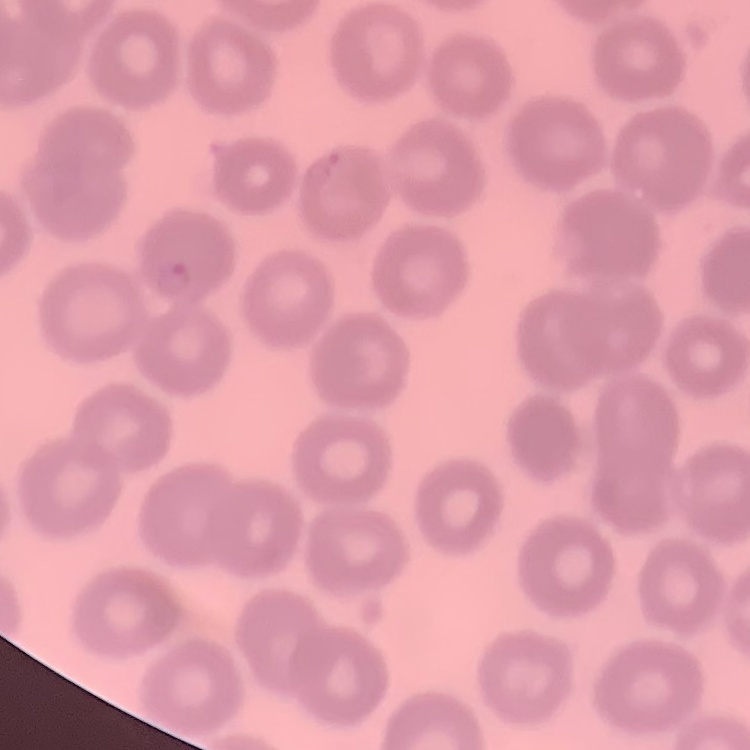

The erythrocytes show no rouleaux formation. Stained with either Field's or Giemsa. Thin blood film. Square crop of a larger photomicrograph.